Locate every uninfected red blood cell.
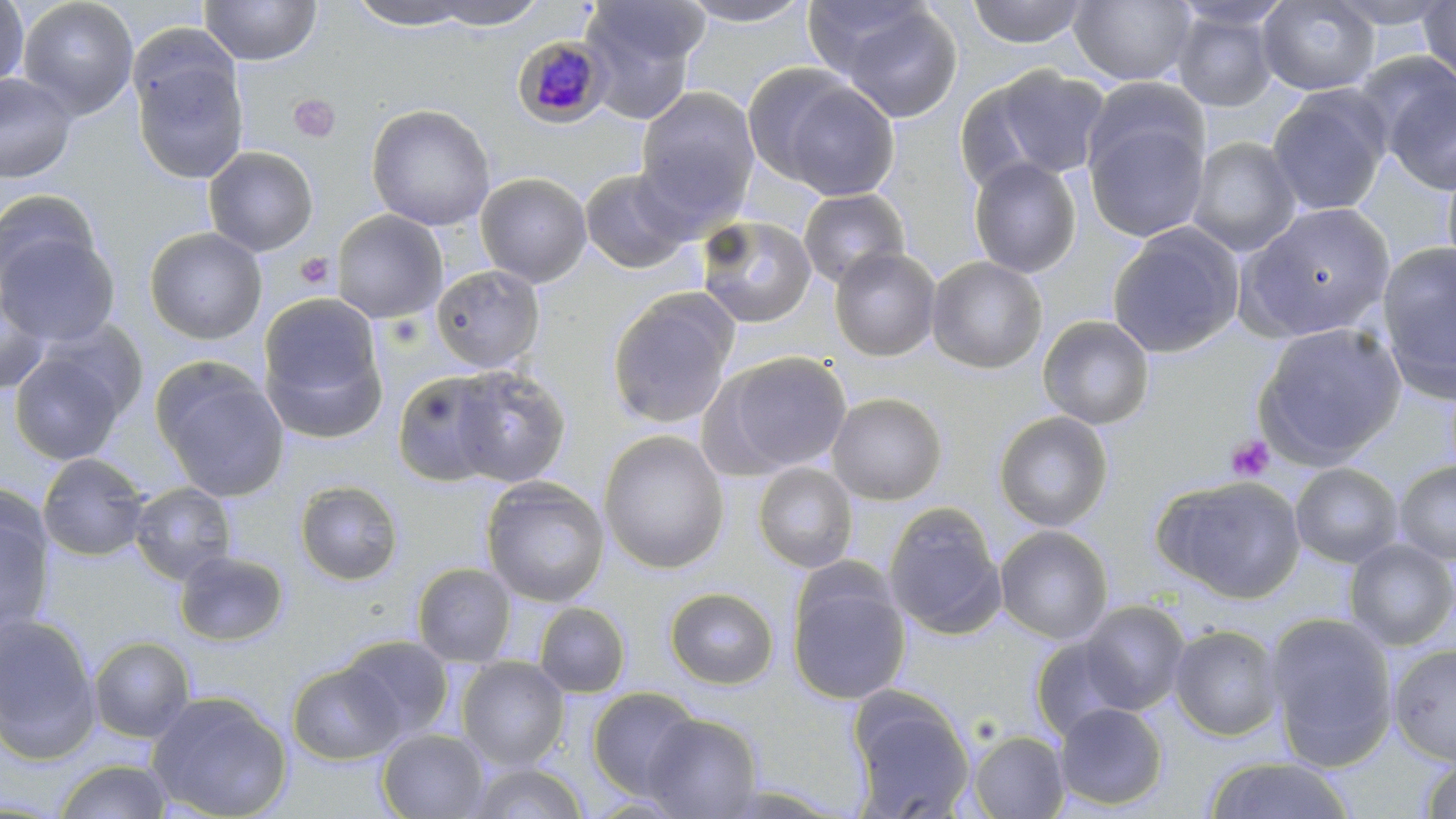

Approximate bounding boxes as named x1/y1/x2/y2 corners in pixels.
Uninfected red blood cells: (x1=0, y1=0, x2=29, y2=92), (x1=18, y1=0, x2=139, y2=119), (x1=199, y1=0, x2=322, y2=66), (x1=344, y1=0, x2=483, y2=30), (x1=423, y1=0, x2=549, y2=30), (x1=579, y1=0, x2=707, y2=117), (x1=677, y1=0, x2=816, y2=27), (x1=802, y1=0, x2=930, y2=80), (x1=965, y1=0, x2=1089, y2=48), (x1=1068, y1=0, x2=1196, y2=87), (x1=1257, y1=0, x2=1381, y2=96), (x1=1327, y1=0, x2=1455, y2=29), (x1=1417, y1=1, x2=1456, y2=87), (x1=1171, y1=6, x2=1280, y2=112), (x1=838, y1=7, x2=964, y2=124), (x1=130, y1=49, x2=249, y2=184), (x1=1378, y1=63, x2=1456, y2=196), (x1=967, y1=65, x2=1113, y2=186), (x1=0, y1=73, x2=77, y2=183), (x1=1085, y1=76, x2=1210, y2=183), (x1=771, y1=78, x2=901, y2=202), (x1=1266, y1=86, x2=1391, y2=217), (x1=634, y1=87, x2=760, y2=226), (x1=366, y1=104, x2=495, y2=231), (x1=1082, y1=113, x2=1210, y2=243), (x1=1186, y1=136, x2=1302, y2=257), (x1=203, y1=146, x2=319, y2=257), (x1=1441, y1=151, x2=1456, y2=282), (x1=968, y1=157, x2=1082, y2=278), (x1=578, y1=168, x2=693, y2=275), (x1=475, y1=172, x2=592, y2=288), (x1=798, y1=188, x2=910, y2=289), (x1=0, y1=189, x2=100, y2=297), (x1=1238, y1=202, x2=1397, y2=342), (x1=332, y1=209, x2=447, y2=323), (x1=695, y1=214, x2=817, y2=329), (x1=1107, y1=223, x2=1245, y2=358), (x1=144, y1=227, x2=266, y2=344), (x1=1, y1=229, x2=120, y2=346), (x1=1377, y1=240, x2=1455, y2=400), (x1=829, y1=247, x2=941, y2=361), (x1=926, y1=256, x2=1048, y2=374), (x1=430, y1=265, x2=546, y2=375), (x1=0, y1=284, x2=52, y2=395), (x1=605, y1=288, x2=740, y2=430), (x1=258, y1=298, x2=388, y2=442), (x1=1037, y1=315, x2=1155, y2=430), (x1=1252, y1=322, x2=1406, y2=468), (x1=10, y1=348, x2=130, y2=465), (x1=705, y1=350, x2=852, y2=479), (x1=153, y1=362, x2=289, y2=501), (x1=448, y1=365, x2=571, y2=488), (x1=391, y1=369, x2=506, y2=487), (x1=826, y1=392, x2=947, y2=505), (x1=993, y1=410, x2=1113, y2=532), (x1=598, y1=429, x2=730, y2=575), (x1=37, y1=453, x2=150, y2=561), (x1=1394, y1=460, x2=1456, y2=564), (x1=752, y1=462, x2=858, y2=574), (x1=1289, y1=462, x2=1404, y2=568), (x1=1153, y1=475, x2=1306, y2=603), (x1=480, y1=477, x2=610, y2=607), (x1=294, y1=479, x2=405, y2=586), (x1=129, y1=482, x2=237, y2=585), (x1=0, y1=499, x2=56, y2=638), (x1=883, y1=502, x2=1005, y2=637), (x1=994, y1=525, x2=1114, y2=645), (x1=1343, y1=538, x2=1456, y2=651), (x1=174, y1=549, x2=289, y2=647), (x1=411, y1=562, x2=517, y2=667), (x1=787, y1=567, x2=911, y2=706), (x1=664, y1=587, x2=779, y2=689), (x1=1077, y1=600, x2=1191, y2=715), (x1=533, y1=602, x2=631, y2=697), (x1=1265, y1=611, x2=1398, y2=771), (x1=0, y1=613, x2=101, y2=764), (x1=1168, y1=624, x2=1285, y2=741), (x1=338, y1=635, x2=456, y2=741), (x1=89, y1=636, x2=196, y2=742), (x1=1029, y1=637, x2=1132, y2=742), (x1=1388, y1=643, x2=1456, y2=765), (x1=456, y1=657, x2=570, y2=771), (x1=287, y1=662, x2=403, y2=765), (x1=588, y1=686, x2=702, y2=800), (x1=847, y1=687, x2=974, y2=818), (x1=147, y1=691, x2=292, y2=819), (x1=1053, y1=702, x2=1168, y2=810), (x1=643, y1=713, x2=762, y2=818), (x1=377, y1=729, x2=491, y2=818), (x1=968, y1=730, x2=1071, y2=818), (x1=1200, y1=755, x2=1357, y2=818), (x1=1419, y1=756, x2=1456, y2=818), (x1=53, y1=758, x2=176, y2=819), (x1=465, y1=761, x2=590, y2=819).

Summary:
  - Platelet locations: (x1=288, y1=93, x2=340, y2=143), (x1=296, y1=253, x2=334, y2=289), (x1=1225, y1=435, x2=1274, y2=482)
  - Plasmodium malariae-infected red blood cell locations: (x1=514, y1=35, x2=611, y2=128)
  - Slide-level diagnosis: Plasmodium malariae
  - Magnification: 1000x
  - Modality: optical microscopy
  - Image size: 1456×819 pixels
  - Stain: May-Grünwald-Giemsa
  - Field of view: single
  - Preparation: thin blood film